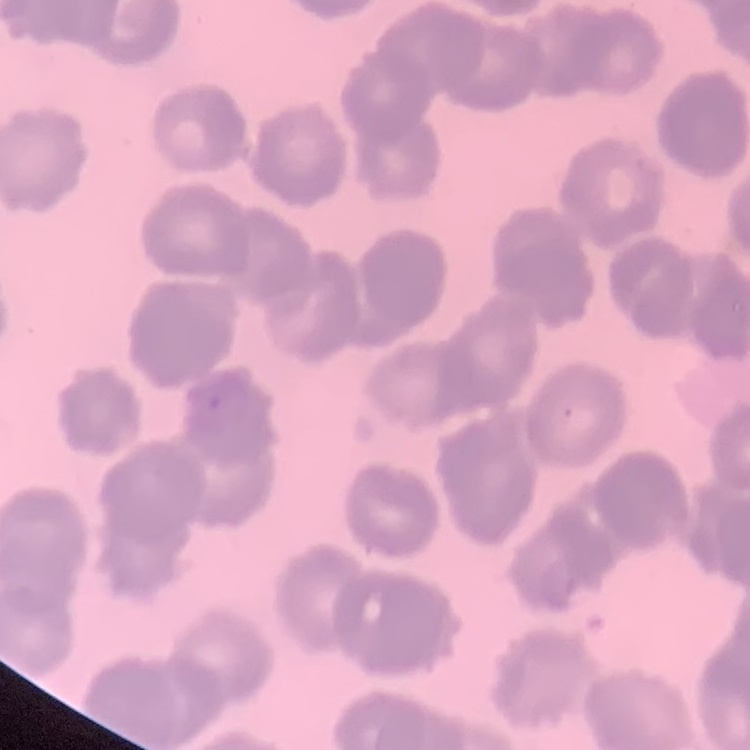

Summary:
  - Erythrocyte morphology: rouleaux formation
  - Preparation: thin peripheral smear
  - Stain: Field's or Giemsa
  - Image type: square crop of a larger photomicrograph